Give the position of every Plasmodium parasite.
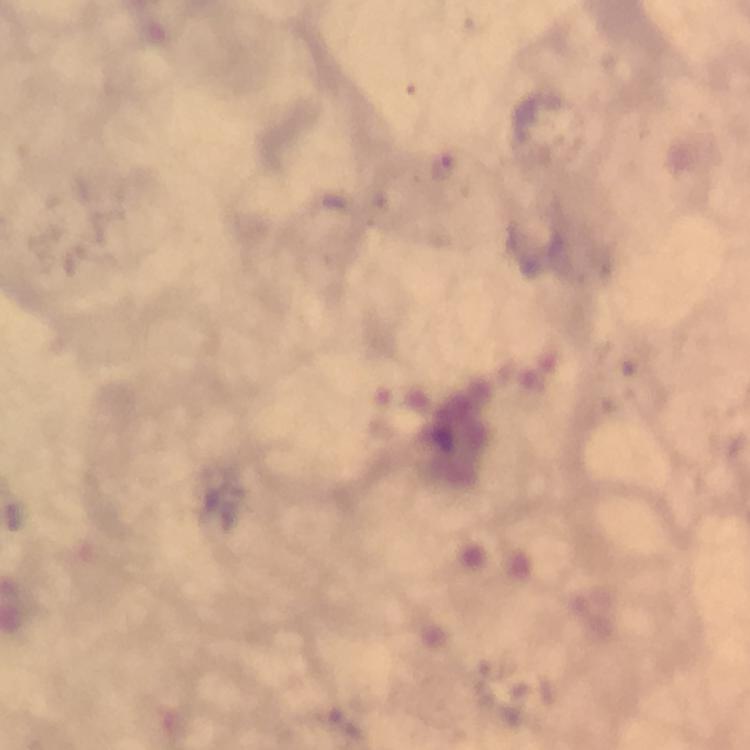
Approximate centers as {x, y} in pixels.
Plasmodium parasites: {444, 168}.

Summary:
  - Cropped from: one field of view
  - Preparation: thick blood smear
  - Image size: 750×750 pixels
  - Context: from a diagnostic examination for malaria
  - Immersion oil: applied
  - Magnification: 100x
  - Capture: smartphone camera through the microscope
  - Stain: Giemsa